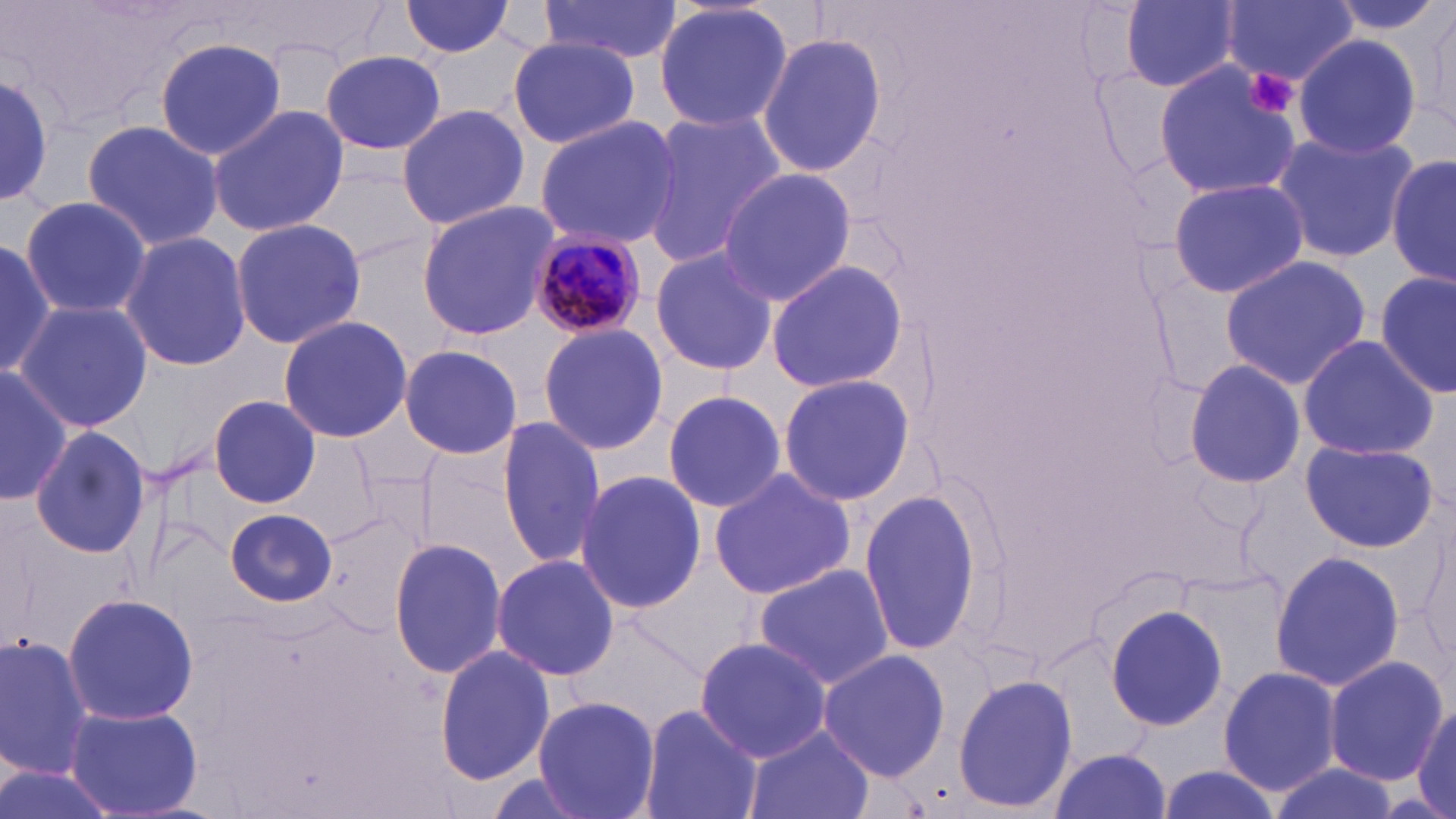

{
  "slide_level_diagnosis": "Plasmodium malariae",
  "magnification": "1000x",
  "uninfected_red_blood_cell_locations": "approximate bounding boxes as named x1/y1/x2/y2 corners in pixels: (x1=398, y1=0, x2=517, y2=57), (x1=538, y1=0, x2=682, y2=64), (x1=1121, y1=0, x2=1241, y2=91), (x1=1322, y1=0, x2=1449, y2=37), (x1=653, y1=1, x2=793, y2=133), (x1=1221, y1=1, x2=1358, y2=86), (x1=1414, y1=1, x2=1455, y2=134), (x1=758, y1=32, x2=886, y2=178), (x1=1290, y1=34, x2=1424, y2=160), (x1=508, y1=37, x2=640, y2=149), (x1=155, y1=38, x2=288, y2=160), (x1=321, y1=50, x2=446, y2=156), (x1=1153, y1=59, x2=1302, y2=204), (x1=1, y1=70, x2=55, y2=210), (x1=396, y1=102, x2=530, y2=232), (x1=206, y1=104, x2=348, y2=239), (x1=638, y1=111, x2=785, y2=269), (x1=532, y1=116, x2=681, y2=248), (x1=81, y1=121, x2=225, y2=248), (x1=1269, y1=130, x2=1419, y2=267), (x1=1388, y1=153, x2=1454, y2=287), (x1=305, y1=160, x2=438, y2=269), (x1=716, y1=168, x2=855, y2=308), (x1=1168, y1=178, x2=1311, y2=300), (x1=18, y1=194, x2=152, y2=318), (x1=416, y1=200, x2=560, y2=340), (x1=229, y1=218, x2=367, y2=350), (x1=0, y1=231, x2=56, y2=381), (x1=120, y1=231, x2=253, y2=372), (x1=650, y1=245, x2=778, y2=378), (x1=1219, y1=256, x2=1371, y2=389), (x1=765, y1=260, x2=910, y2=394), (x1=1375, y1=269, x2=1455, y2=397), (x1=13, y1=301, x2=154, y2=431), (x1=277, y1=313, x2=412, y2=443), (x1=536, y1=321, x2=668, y2=456), (x1=1297, y1=336, x2=1437, y2=460), (x1=397, y1=344, x2=523, y2=459), (x1=1182, y1=357, x2=1307, y2=490), (x1=0, y1=364, x2=72, y2=506), (x1=777, y1=373, x2=917, y2=504), (x1=660, y1=392, x2=789, y2=514), (x1=208, y1=393, x2=322, y2=508), (x1=495, y1=417, x2=610, y2=569), (x1=28, y1=424, x2=152, y2=561), (x1=1300, y1=438, x2=1439, y2=554), (x1=708, y1=466, x2=856, y2=600), (x1=574, y1=469, x2=705, y2=615), (x1=861, y1=492, x2=981, y2=655), (x1=224, y1=509, x2=338, y2=608), (x1=1406, y1=516, x2=1454, y2=676), (x1=389, y1=536, x2=509, y2=680), (x1=1267, y1=549, x2=1405, y2=696), (x1=490, y1=554, x2=621, y2=682), (x1=753, y1=566, x2=893, y2=689), (x1=63, y1=591, x2=198, y2=726), (x1=1104, y1=602, x2=1230, y2=732), (x1=573, y1=611, x2=711, y2=735), (x1=0, y1=634, x2=94, y2=777), (x1=692, y1=635, x2=832, y2=761), (x1=435, y1=644, x2=555, y2=785), (x1=817, y1=648, x2=951, y2=781), (x1=1322, y1=656, x2=1449, y2=786), (x1=1218, y1=666, x2=1343, y2=794), (x1=953, y1=673, x2=1077, y2=812), (x1=533, y1=696, x2=660, y2=819), (x1=1412, y1=699, x2=1455, y2=819), (x1=64, y1=702, x2=201, y2=819), (x1=636, y1=704, x2=762, y2=819), (x1=743, y1=724, x2=877, y2=819), (x1=1049, y1=751, x2=1172, y2=819), (x1=0, y1=757, x2=120, y2=819), (x1=1263, y1=763, x2=1398, y2=819), (x1=1154, y1=767, x2=1284, y2=819)",
  "modality": "optical microscopy",
  "preparation": "thin blood film",
  "stain": "May-Grünwald-Giemsa",
  "image_size": "1456×819 pixels",
  "plasmodium_malariae_infected_red_blood_cell_locations": "approximate bounding boxes as named x1/y1/x2/y2 corners in pixels: (x1=526, y1=231, x2=649, y2=340)",
  "platelet_locations": "approximate bounding boxes as named x1/y1/x2/y2 corners in pixels: (x1=1242, y1=68, x2=1299, y2=119)",
  "field_of_view": "single"
}